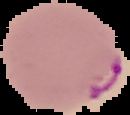

Summary:
  - Image size: 130×115 pixels
  - Preparation: thin blood smear
  - Malaria status: parasitized
  - Image type: cell region segmented out of the field of view; surrounding area masked to black